Name the cell type shown.
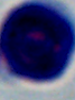

This is a leukocyte.

modality: micrograph
magnification: 1000x